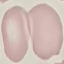 Result: negative for malaria parasites. Thin blood smear. Automatically extracted cell patch, resized to 64 × 64 pixels. Giemsa stain. Photographed with a smartphone camera at the microscope eyepiece.